Describe the morphology of the red blood cells.
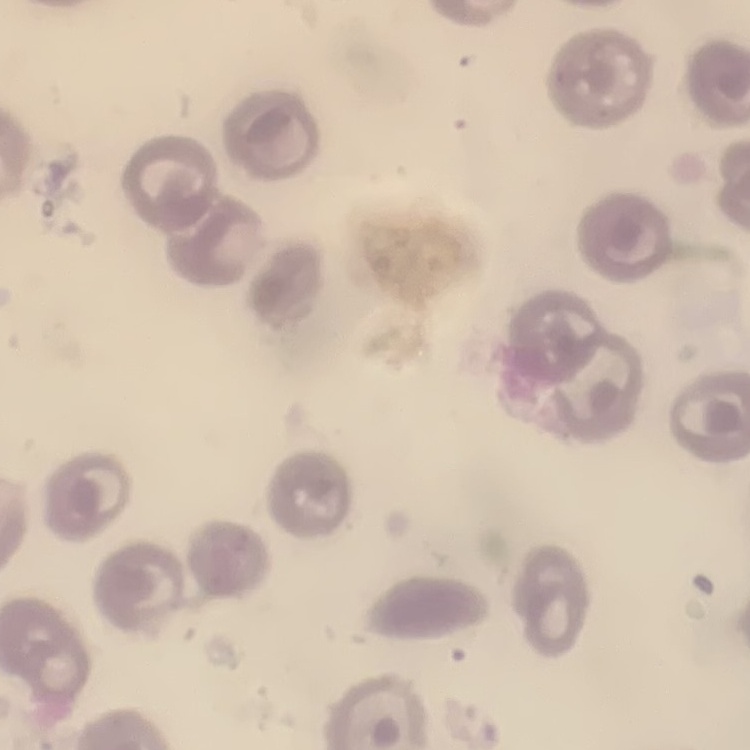

No rouleaux formation.

image type = one tile cut from a larger photomicrograph
stain = Field's or Giemsa
preparation = thin blood film